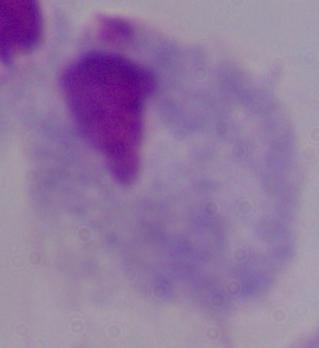 1000x magnification. A trichomonad is seen. Photomicrograph.